State which parasite is depicted.
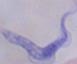

This is a trypanosome.

{
  "magnification": "1000x",
  "modality": "photomicrograph"
}